Identify the preparation type.
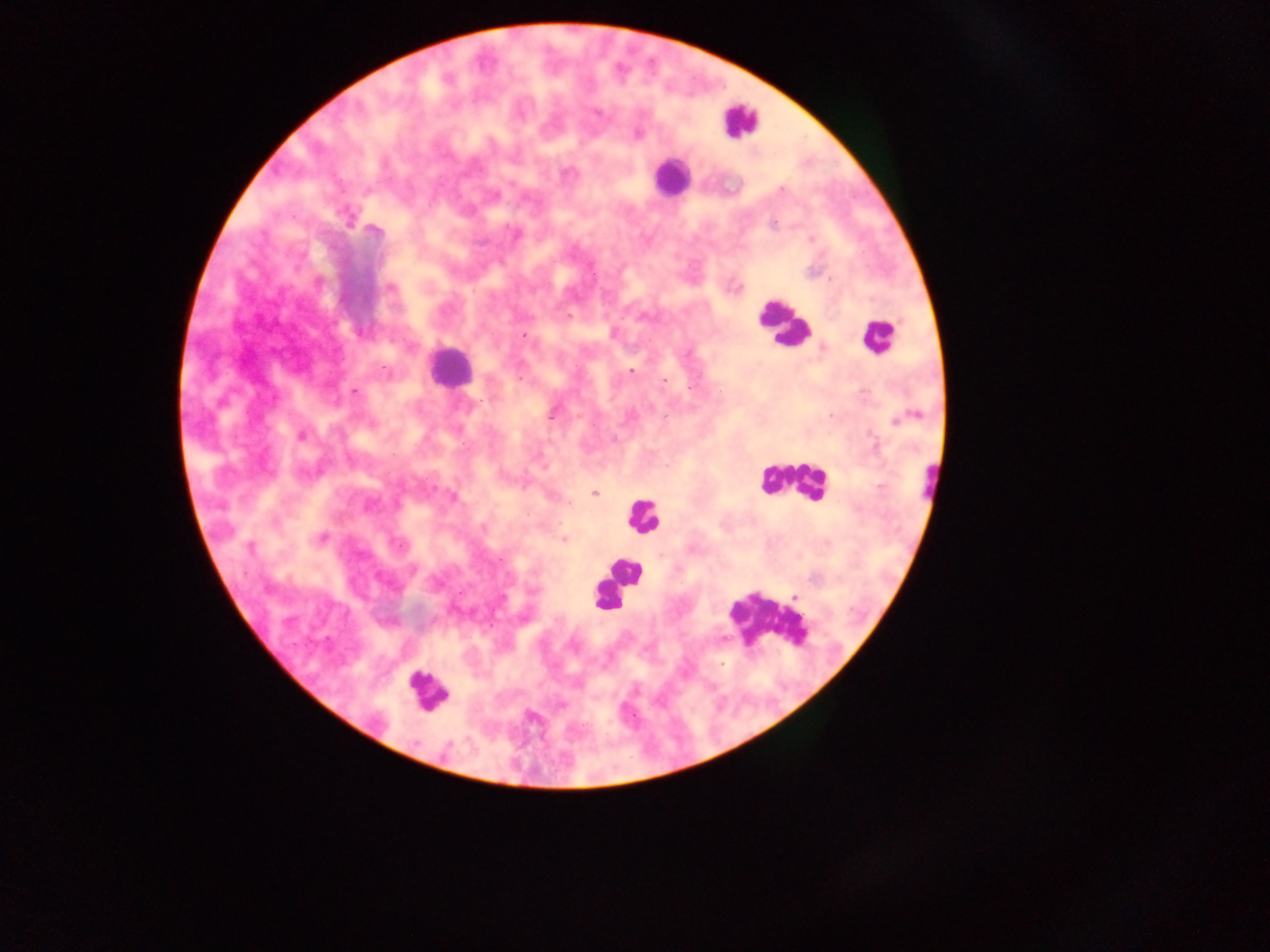

This is a thick smear.

Approximate centers as [x, y] in pixels. Malaria parasite locations: [447, 79], [598, 112], [638, 134], [782, 189], [774, 224], [374, 231], [390, 288], [736, 288], [568, 316], [523, 335], [821, 348], [631, 370], [664, 381], [690, 387], [353, 391], [552, 415], [301, 436], [594, 492], [570, 504], [320, 539], [563, 540], [399, 545], [250, 548], [500, 561]. Leukocyte locations: [739, 120], [670, 177], [783, 325], [878, 337], [448, 366], [793, 481], [929, 483], [642, 514], [624, 572], [616, 582], [607, 597], [766, 618], [426, 691]. Single field of view. Image is 1270×952 pixels. Photographed through a microscope with a mobile-phone camera. Sample from Ghana.